Identify the blood parasite species.
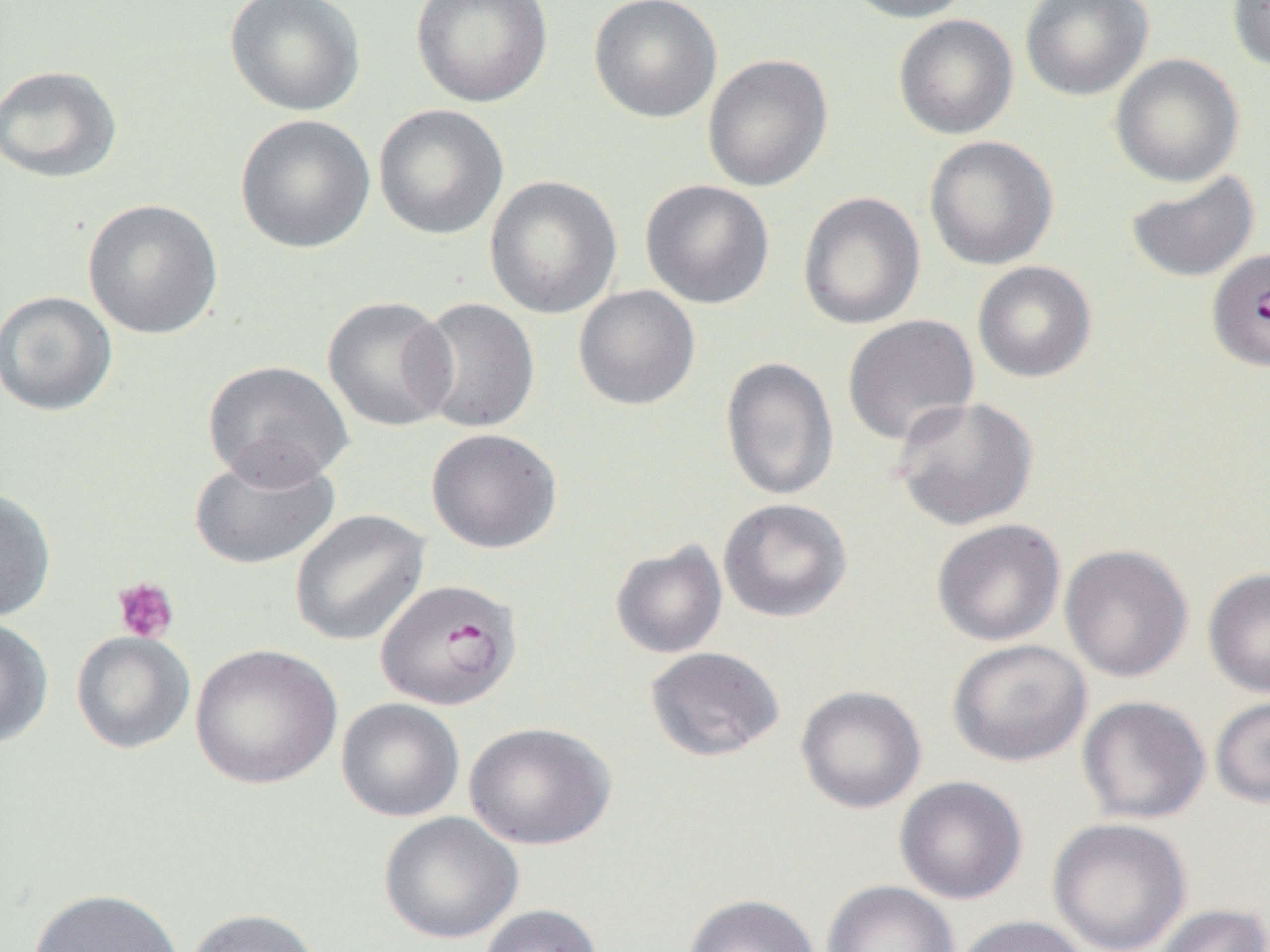

Plasmodium falciparum.

modality = light microscopy
Plasmodium falciparum-infected red blood cell locations = approximate bounding boxes as [x1, y1, x2, y2] in pixels: [1212, 249, 1270, 373], [374, 578, 522, 711]
preparation = thin blood smear
uninfected red blood cell locations = approximate bounding boxes as [x1, y1, x2, y2] in pixels: [224, 0, 365, 117], [411, 0, 552, 107], [589, 0, 722, 123], [841, 0, 976, 23], [1019, 0, 1153, 101], [1227, 0, 1270, 72], [893, 14, 1019, 140], [1110, 53, 1244, 187], [701, 54, 834, 192], [0, 65, 122, 183], [373, 104, 509, 240], [235, 114, 376, 254], [924, 135, 1058, 270], [1126, 170, 1260, 283], [484, 175, 622, 319], [640, 179, 775, 309], [797, 191, 925, 330], [82, 199, 223, 340], [972, 261, 1097, 382], [573, 285, 700, 410], [0, 290, 117, 417], [322, 296, 457, 433], [411, 296, 540, 435], [842, 315, 979, 446], [720, 356, 839, 501], [202, 360, 354, 489], [891, 396, 1039, 531], [426, 428, 562, 553], [188, 447, 340, 570], [0, 486, 57, 623], [718, 498, 853, 622], [290, 509, 430, 647], [931, 518, 1066, 647], [610, 540, 728, 659], [1059, 543, 1193, 683], [1203, 567, 1270, 698], [0, 616, 54, 749], [71, 631, 195, 754], [948, 639, 1092, 767], [190, 643, 343, 790], [645, 646, 784, 761], [795, 685, 927, 813], [1077, 695, 1211, 825], [1210, 695, 1270, 809], [336, 698, 465, 822], [464, 721, 616, 850], [894, 775, 1028, 905], [378, 811, 523, 944], [1047, 817, 1192, 951], [822, 880, 960, 952], [27, 887, 186, 952], [683, 893, 821, 952], [479, 903, 605, 952], [1151, 904, 1270, 952], [183, 908, 323, 952], [953, 915, 1091, 952]
image size = 1270×952 pixels
magnification = 1000x
platelet locations = approximate bounding boxes as [x1, y1, x2, y2] in pixels: [112, 576, 179, 643]
field of view = single